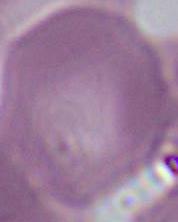
Summary:
  - Identification: red blood cell
  - Magnification: 1000x
  - Modality: micrograph